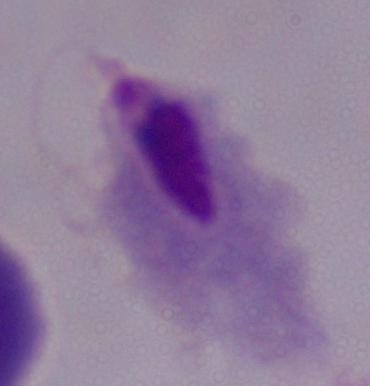

Summary:
  - Identification: trichomonad
  - Modality: micrograph
  - Magnification: 1000x